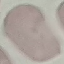

malaria status = uninfected
image type = automatically extracted cell patch, resized to 64 × 64 pixels
capture = smartphone camera at the microscope eyepiece
stain = Giemsa
preparation = thin smear